Give the position of each P. falciparum parasite with its life-cycle stage, each leukocyte, and any debris.
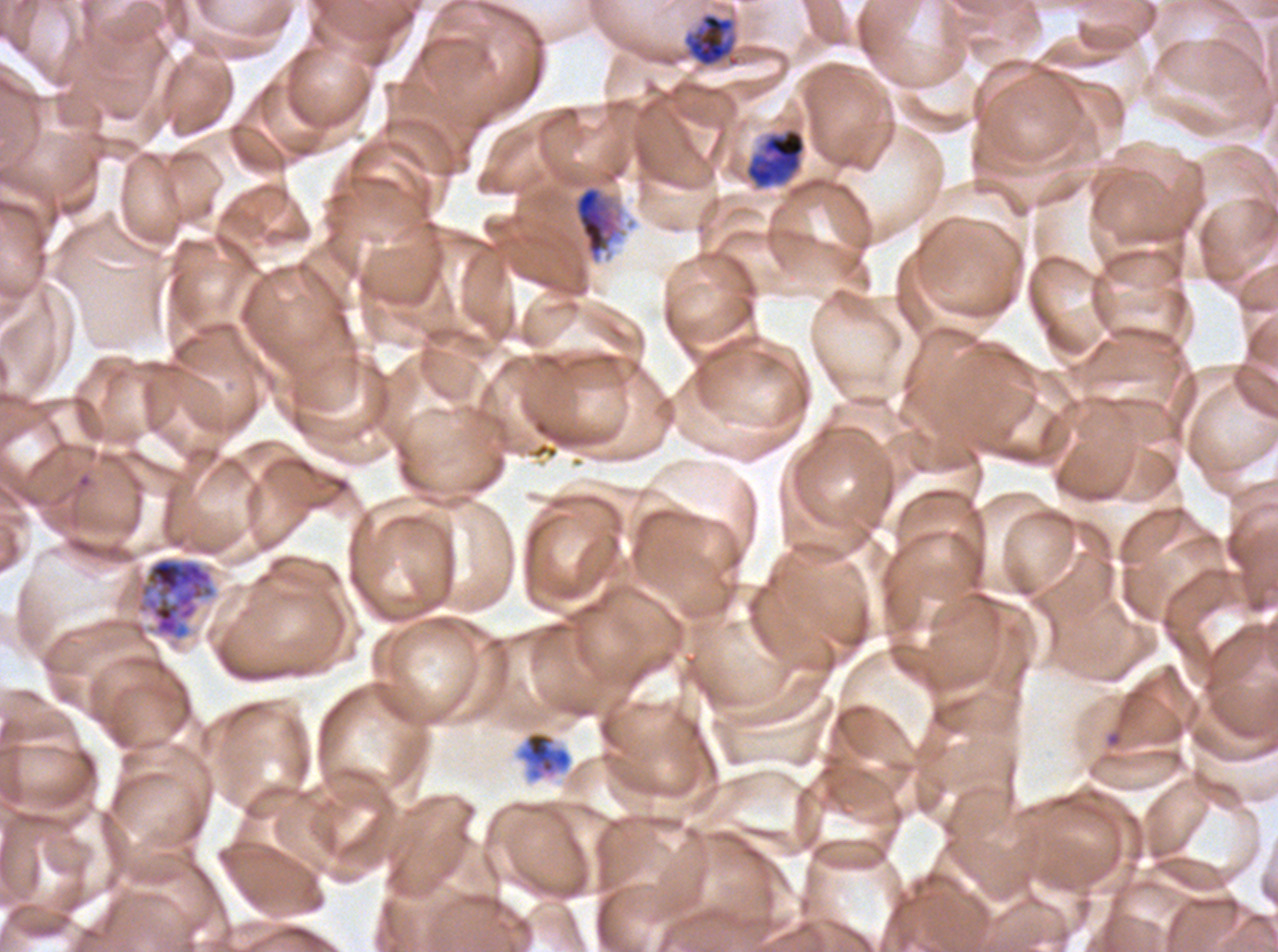

Approximate bounding rectangles given as corner coordinates in pixels from the top-left.
Late trophozoites: (x1=682, y1=12, x2=741, y2=67), (x1=515, y1=729, x2=573, y2=783).
Early schizonts: (x1=744, y1=127, x2=806, y2=190), (x1=573, y1=185, x2=619, y2=261), (x1=135, y1=555, x2=216, y2=641).
No rings, late-ring/early-trophozoite forms, mid trophozoites, late schizonts, segmenters, gametocytes, leukocytes, or debris observed.

Summary:
  - Image size: 1278×952 pixels
  - Life-cycle stages observed: late trophozoite, early schizont
  - Specimen: P. falciparum from a patient in The Gambia, cultured ex vivo for 24 to 48 hours
  - Stain: Giemsa
  - Preparation: thin blood smear
  - Field of view: one sub-image of a larger composite